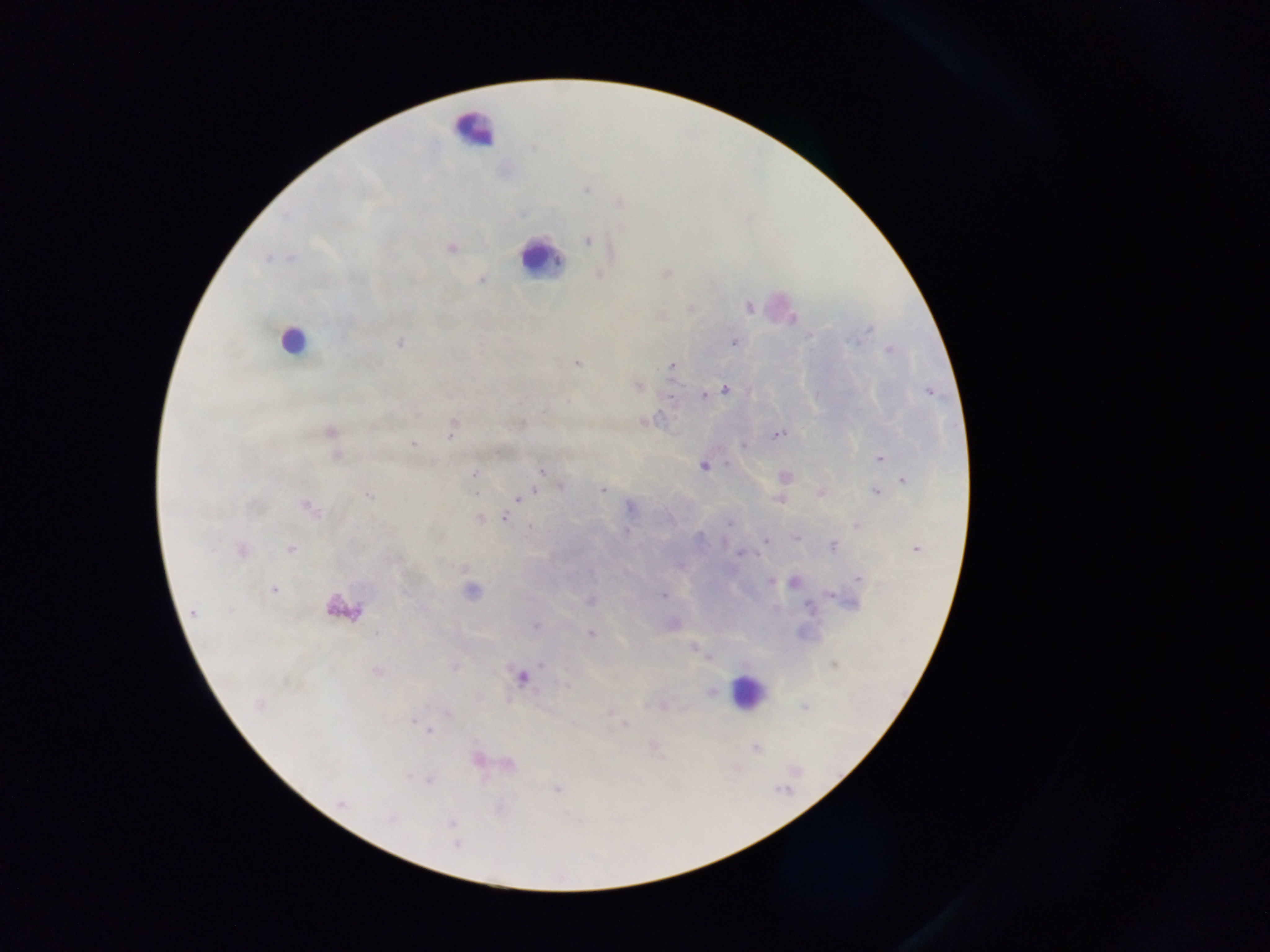
Approximate centers as {x, y} in pixels. Leukocyte locations: {473, 130}, {539, 258}, {292, 341}, {345, 608}, {747, 691}. Plasmodium parasite locations: {618, 203}, {587, 240}, {450, 248}, {665, 273}, {599, 275}, {480, 279}, {748, 307}, {400, 342}, {733, 342}, {889, 350}, {576, 362}, {672, 366}, {638, 386}, {725, 389}, {930, 391}, {703, 394}, {644, 421}, {520, 423}, {452, 426}, {329, 431}, {778, 434}, {413, 442}, {744, 446}, {337, 456}, {879, 457}, {703, 465}, {541, 471}, {475, 474}, {783, 476}, {903, 479}, {560, 486}, {603, 489}, {876, 491}, {821, 492}, {369, 495}, {518, 498}, {781, 498}, {309, 507}, {630, 507}, {505, 518}, {479, 519}, {857, 525}, {627, 531}, {796, 537}, {766, 540}, {833, 545}, {241, 549}, {290, 549}, {916, 549}, {741, 552}, {679, 565}, {465, 568}, {857, 578}, {771, 581}, {793, 581}, {273, 590}, {472, 591}, {663, 596}, {590, 600}, {194, 612}, {671, 624}, {536, 626}, {591, 633}, {693, 646}, {710, 657}, {454, 667}, {378, 671}, {521, 676}, {568, 685}, {711, 692}, {259, 703}, {662, 706}, {804, 707}, {447, 712}, {608, 712}, {414, 719}, {623, 725}, {428, 732}, {653, 746}, {755, 748}, {477, 759}, {506, 763}, {429, 779}, {556, 788}, {341, 804}, {452, 823}, {456, 845}. Thick blood smear. Mobile-phone photograph taken through the microscope. Image is 1270×952 pixels. Collected in Ghana. Single field of view.